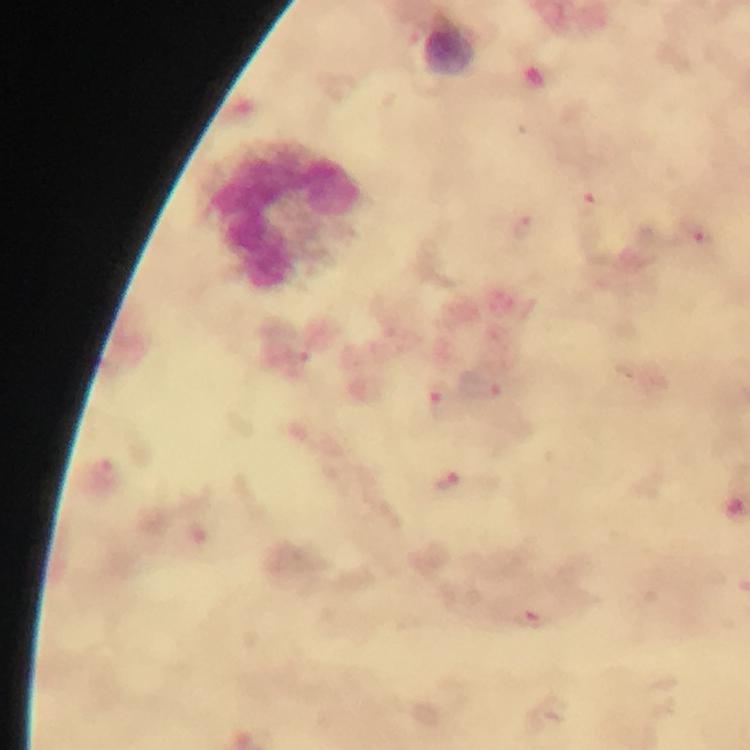

Approximate centers as {x, y} in pixels.
Summary:
  - Leukocyte locations: {450, 50}, {286, 218}
  - Malaria parasite locations: {589, 204}, {522, 227}, {700, 236}, {298, 353}, {481, 384}, {440, 398}, {449, 483}, {534, 619}
  - Magnification: 100x
  - Immersion oil: applied
  - Capture: smartphone photograph through a microscope
  - Stain: Giemsa
  - Cropped from: a single field of view
  - Context: from a diagnostic examination for malaria
  - Image size: 750×750 pixels
  - Preparation: thick blood smear